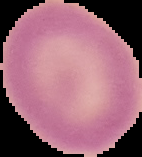

From a thin blood smear. Result: negative for Plasmodium parasites. Image is 142×157 pixels. The area outside the segmented cell region is set to black.